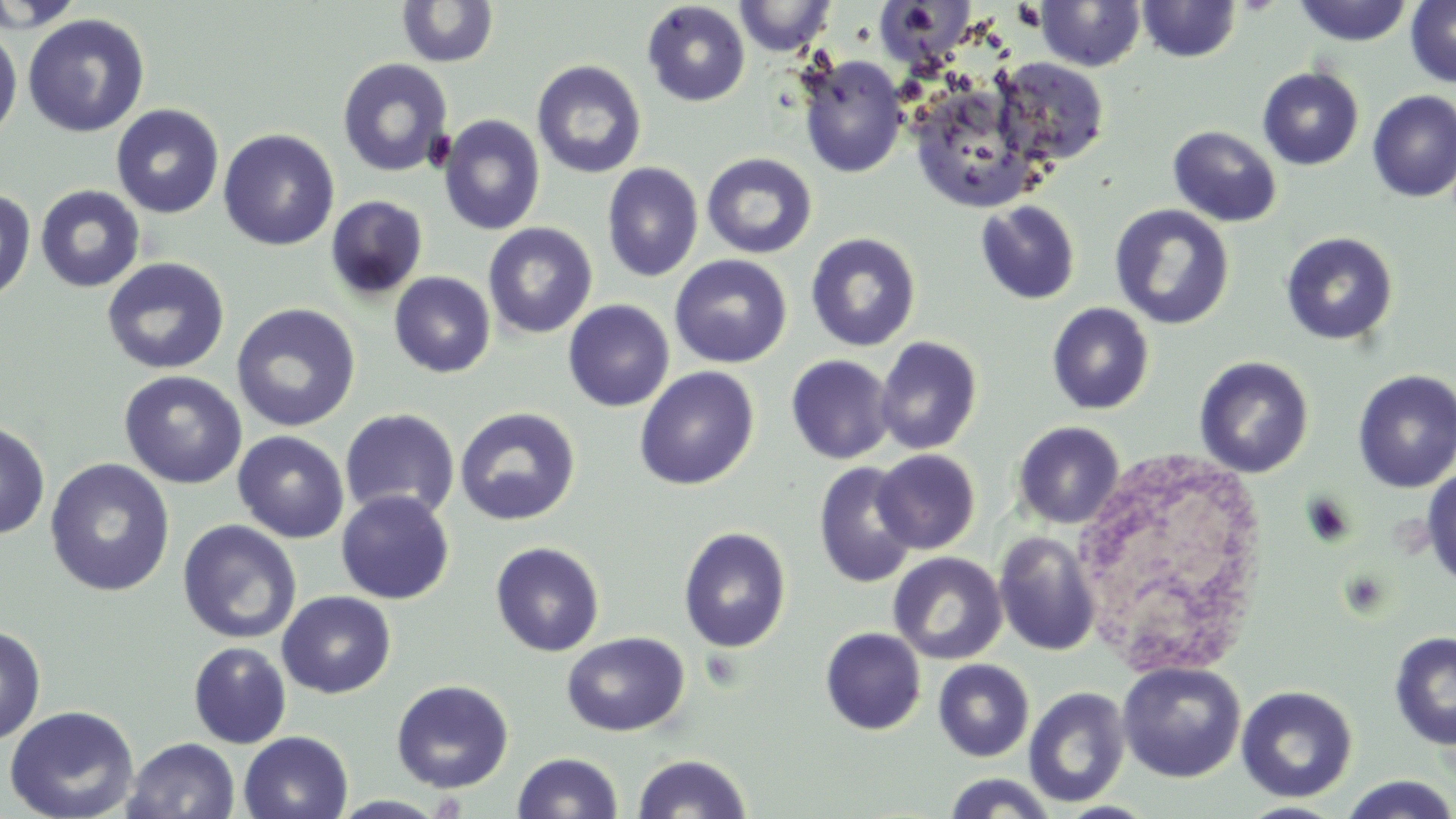

Approximate bounding boxes as named x1/y1/x2/y2 corners in pixels. White blood cell locations: (x1=1078, y1=447, x2=1260, y2=672). Uninfected red blood cell locations: (x1=0, y1=0, x2=88, y2=32), (x1=734, y1=0, x2=837, y2=56), (x1=1034, y1=0, x2=1147, y2=71), (x1=1137, y1=0, x2=1242, y2=63), (x1=1293, y1=0, x2=1413, y2=46), (x1=1405, y1=0, x2=1456, y2=88), (x1=396, y1=1, x2=498, y2=68), (x1=642, y1=2, x2=751, y2=107), (x1=22, y1=14, x2=150, y2=137), (x1=0, y1=25, x2=22, y2=144), (x1=796, y1=54, x2=908, y2=178), (x1=991, y1=57, x2=1110, y2=168), (x1=337, y1=58, x2=454, y2=178), (x1=531, y1=60, x2=647, y2=179), (x1=1258, y1=67, x2=1364, y2=171), (x1=907, y1=82, x2=1045, y2=212), (x1=1367, y1=91, x2=1456, y2=202), (x1=111, y1=104, x2=225, y2=219), (x1=438, y1=114, x2=545, y2=235), (x1=1168, y1=126, x2=1282, y2=227), (x1=218, y1=129, x2=339, y2=250), (x1=701, y1=152, x2=818, y2=260), (x1=601, y1=161, x2=704, y2=282), (x1=34, y1=184, x2=145, y2=293), (x1=0, y1=190, x2=36, y2=304), (x1=325, y1=195, x2=428, y2=301), (x1=975, y1=200, x2=1081, y2=305), (x1=1109, y1=204, x2=1236, y2=330), (x1=483, y1=222, x2=597, y2=339), (x1=1280, y1=231, x2=1399, y2=345), (x1=805, y1=232, x2=921, y2=352), (x1=669, y1=254, x2=792, y2=368), (x1=101, y1=257, x2=230, y2=375), (x1=389, y1=271, x2=496, y2=378), (x1=563, y1=300, x2=675, y2=412), (x1=1046, y1=302, x2=1154, y2=415), (x1=230, y1=303, x2=361, y2=433), (x1=874, y1=335, x2=983, y2=455), (x1=786, y1=354, x2=895, y2=464), (x1=1194, y1=355, x2=1314, y2=478), (x1=634, y1=366, x2=759, y2=491), (x1=118, y1=370, x2=247, y2=489), (x1=1352, y1=370, x2=1456, y2=492), (x1=454, y1=407, x2=581, y2=526), (x1=339, y1=409, x2=460, y2=521), (x1=0, y1=420, x2=50, y2=539), (x1=1012, y1=421, x2=1125, y2=529), (x1=232, y1=431, x2=349, y2=543), (x1=872, y1=449, x2=980, y2=554), (x1=44, y1=457, x2=176, y2=597), (x1=814, y1=461, x2=919, y2=589), (x1=1421, y1=466, x2=1456, y2=590), (x1=336, y1=490, x2=454, y2=604), (x1=176, y1=519, x2=302, y2=644), (x1=678, y1=526, x2=792, y2=653), (x1=994, y1=532, x2=1102, y2=656), (x1=490, y1=541, x2=605, y2=657), (x1=888, y1=552, x2=1007, y2=665), (x1=277, y1=590, x2=396, y2=699), (x1=0, y1=625, x2=46, y2=746), (x1=820, y1=627, x2=926, y2=735), (x1=561, y1=631, x2=690, y2=737), (x1=1389, y1=631, x2=1456, y2=751), (x1=188, y1=641, x2=292, y2=748), (x1=933, y1=659, x2=1034, y2=762), (x1=1117, y1=660, x2=1246, y2=782), (x1=391, y1=679, x2=515, y2=793), (x1=1236, y1=685, x2=1358, y2=802), (x1=1023, y1=686, x2=1131, y2=808), (x1=3, y1=704, x2=140, y2=819), (x1=239, y1=731, x2=353, y2=819), (x1=124, y1=736, x2=240, y2=819), (x1=513, y1=751, x2=623, y2=819), (x1=632, y1=753, x2=752, y2=818), (x1=941, y1=773, x2=1060, y2=818), (x1=1338, y1=775, x2=1456, y2=819). Slide-level diagnosis: negative for blood parasites. May-Grünwald-Giemsa stain. Single field of view. 1000x magnification. Image is 1456×819 pixels. Thin blood smear. Optical microscopy.